Identify the blood parasite species.
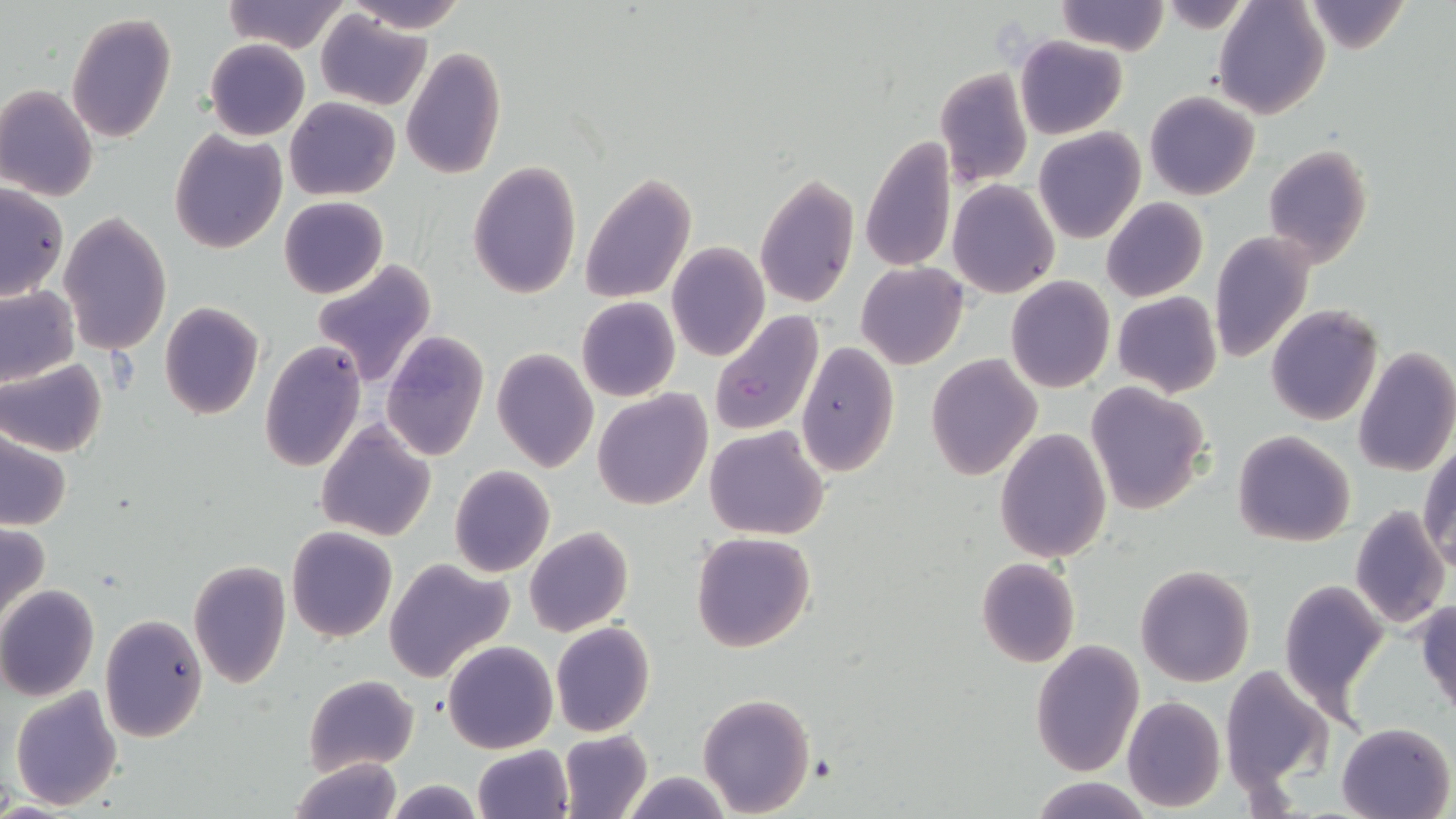

Plasmodium falciparum.

Approximate bounding boxes as (x1, y1, x2, y2) in pixels. Uninfected red blood cell locations: (221, 0, 349, 53), (346, 0, 469, 32), (1054, 0, 1170, 54), (1212, 0, 1332, 119), (1300, 1, 1411, 54), (316, 9, 430, 110), (66, 12, 176, 144), (1014, 36, 1127, 139), (205, 37, 310, 141), (400, 48, 506, 179), (933, 66, 1033, 189), (0, 84, 99, 201), (1144, 90, 1260, 201), (284, 97, 399, 200), (1033, 127, 1145, 244), (169, 129, 287, 255), (860, 135, 956, 274), (1262, 144, 1373, 268), (467, 161, 581, 299), (754, 172, 858, 310), (579, 173, 697, 304), (948, 180, 1060, 299), (0, 184, 68, 302), (279, 196, 388, 298), (1102, 198, 1208, 302), (58, 212, 172, 357), (1209, 231, 1315, 363), (667, 242, 769, 363), (312, 259, 437, 388), (856, 262, 968, 369), (1007, 276, 1114, 392), (0, 285, 78, 387), (1112, 291, 1222, 398), (576, 296, 680, 402), (157, 302, 264, 420), (1266, 303, 1382, 426), (379, 329, 489, 462), (259, 340, 367, 472), (796, 340, 900, 477), (493, 346, 600, 473), (1354, 347, 1456, 478), (927, 353, 1041, 480), (1, 360, 106, 457), (1085, 381, 1211, 514), (592, 388, 713, 511), (315, 420, 436, 540), (704, 425, 830, 540), (1, 427, 74, 531), (994, 428, 1112, 563), (1232, 431, 1356, 547), (1420, 442, 1455, 569), (448, 466, 557, 578), (1349, 506, 1451, 632), (0, 520, 51, 631), (524, 526, 633, 637), (286, 527, 397, 642), (690, 531, 817, 653), (383, 557, 514, 683), (975, 558, 1079, 668), (188, 561, 291, 689), (1136, 563, 1255, 687), (1278, 580, 1387, 715), (0, 584, 99, 701), (1414, 599, 1456, 716), (99, 615, 208, 742), (549, 621, 655, 738), (444, 640, 558, 754), (1031, 641, 1144, 776), (1218, 664, 1335, 797), (303, 674, 419, 775), (9, 687, 124, 811), (696, 693, 814, 816), (1121, 695, 1226, 811), (1335, 721, 1456, 818), (558, 730, 652, 819), (472, 745, 574, 819), (290, 755, 402, 819), (619, 771, 734, 818), (1027, 777, 1156, 818), (382, 779, 489, 817). Plasmodium falciparum-infected red blood cell locations: (708, 310, 822, 437). Light microscopy. 1000x magnification. May-Grünwald-Giemsa-stained preparation. One field of a larger specimen. Thin blood smear. Image is 1456×819 pixels.